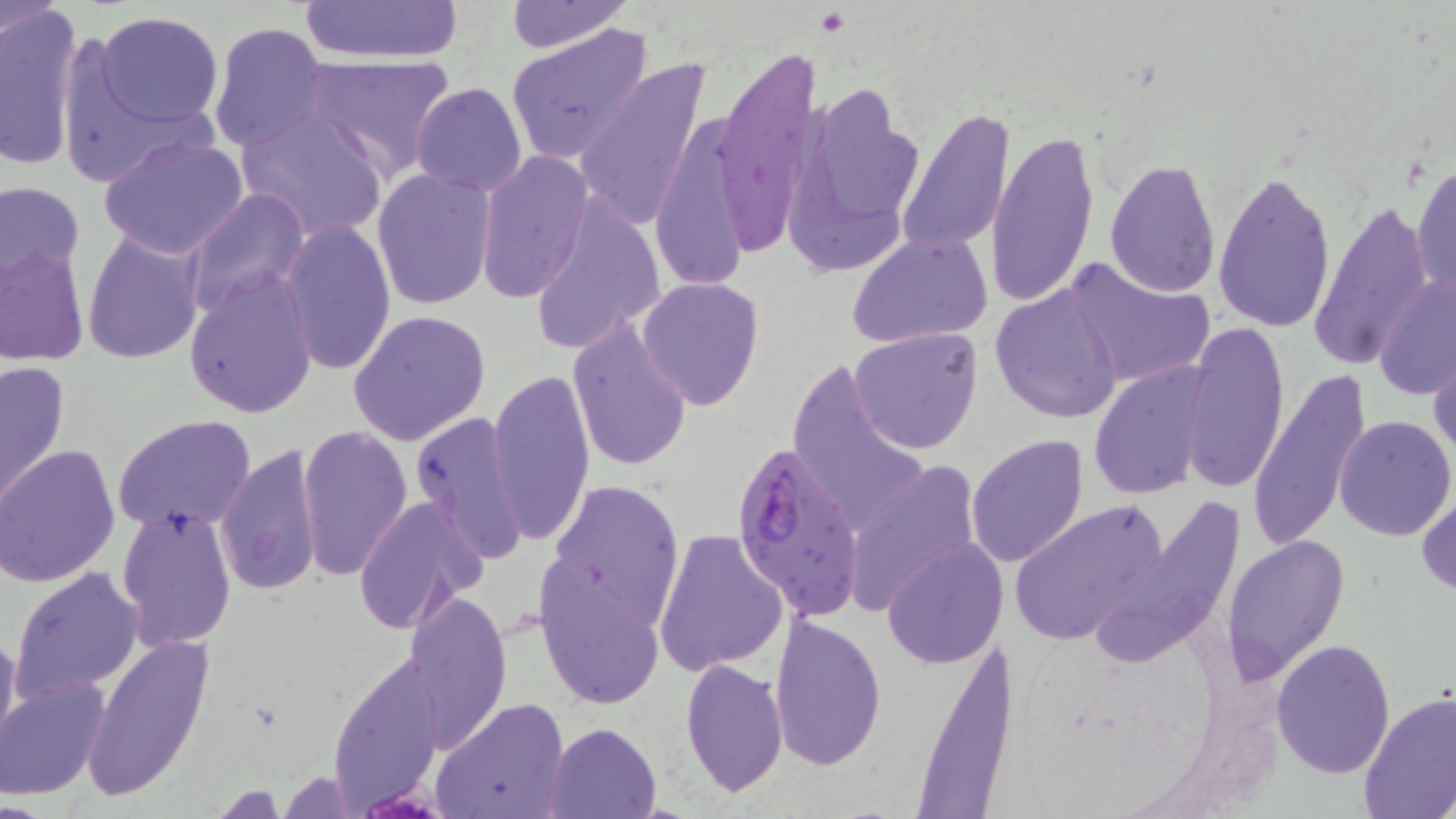

slide-level diagnosis = Plasmodium falciparum
modality = light microscopy
stain = May-Grünwald-Giemsa
magnification = 1000x
platelet locations = approximate bounding boxes as named x1/y1/x2/y2 corners in pixels: (x1=817, y1=8, x2=848, y2=35)
field of view = one of a larger specimen
image size = 1456×819 pixels
uninfected red blood cell locations = approximate bounding boxes as named x1/y1/x2/y2 corners in pixels: (x1=301, y1=0, x2=465, y2=66), (x1=502, y1=1, x2=634, y2=53), (x1=0, y1=2, x2=89, y2=172), (x1=93, y1=11, x2=225, y2=126), (x1=208, y1=21, x2=329, y2=152), (x1=505, y1=23, x2=655, y2=166), (x1=716, y1=48, x2=822, y2=245), (x1=301, y1=52, x2=457, y2=180), (x1=573, y1=58, x2=714, y2=232), (x1=788, y1=80, x2=929, y2=264), (x1=409, y1=83, x2=528, y2=197), (x1=235, y1=108, x2=390, y2=243), (x1=896, y1=108, x2=1018, y2=257), (x1=648, y1=112, x2=771, y2=296), (x1=987, y1=130, x2=1098, y2=308), (x1=98, y1=132, x2=252, y2=260), (x1=476, y1=150, x2=592, y2=303), (x1=1105, y1=158, x2=1221, y2=296), (x1=1412, y1=159, x2=1455, y2=305), (x1=370, y1=166, x2=496, y2=310), (x1=1212, y1=168, x2=1338, y2=333), (x1=0, y1=179, x2=86, y2=295), (x1=182, y1=188, x2=310, y2=319), (x1=523, y1=194, x2=669, y2=356), (x1=1310, y1=202, x2=1433, y2=372), (x1=280, y1=218, x2=395, y2=377), (x1=81, y1=227, x2=204, y2=364), (x1=846, y1=231, x2=993, y2=349), (x1=0, y1=242, x2=89, y2=367), (x1=1061, y1=258, x2=1213, y2=388), (x1=1375, y1=265, x2=1454, y2=406), (x1=183, y1=270, x2=318, y2=420), (x1=637, y1=275, x2=765, y2=409), (x1=990, y1=284, x2=1126, y2=424), (x1=347, y1=309, x2=491, y2=447), (x1=567, y1=317, x2=693, y2=474), (x1=1179, y1=321, x2=1291, y2=493), (x1=850, y1=326, x2=983, y2=454), (x1=1431, y1=342, x2=1456, y2=471), (x1=1, y1=359, x2=71, y2=508), (x1=788, y1=359, x2=929, y2=534), (x1=1088, y1=362, x2=1214, y2=499), (x1=486, y1=364, x2=595, y2=549), (x1=1248, y1=367, x2=1372, y2=548), (x1=407, y1=409, x2=527, y2=561), (x1=112, y1=414, x2=259, y2=535), (x1=1334, y1=414, x2=1454, y2=540), (x1=297, y1=425, x2=413, y2=580), (x1=966, y1=434, x2=1091, y2=568), (x1=216, y1=441, x2=324, y2=596), (x1=0, y1=444, x2=120, y2=587), (x1=839, y1=461, x2=983, y2=616), (x1=546, y1=479, x2=685, y2=628), (x1=1417, y1=490, x2=1456, y2=596), (x1=1093, y1=493, x2=1247, y2=671), (x1=353, y1=496, x2=488, y2=632), (x1=1008, y1=499, x2=1170, y2=645), (x1=116, y1=506, x2=237, y2=651), (x1=653, y1=528, x2=789, y2=676), (x1=1222, y1=531, x2=1349, y2=686), (x1=882, y1=536, x2=1005, y2=668), (x1=534, y1=560, x2=666, y2=710), (x1=10, y1=566, x2=145, y2=702), (x1=402, y1=589, x2=514, y2=752), (x1=767, y1=613, x2=887, y2=771), (x1=0, y1=618, x2=19, y2=755), (x1=79, y1=632, x2=218, y2=801), (x1=1272, y1=638, x2=1396, y2=777), (x1=328, y1=649, x2=447, y2=806), (x1=680, y1=658, x2=789, y2=798), (x1=2, y1=675, x2=109, y2=800), (x1=1357, y1=690, x2=1456, y2=818), (x1=431, y1=697, x2=571, y2=819), (x1=547, y1=721, x2=661, y2=818), (x1=276, y1=771, x2=358, y2=815)
preparation = thin blood smear
Plasmodium falciparum-infected red blood cell locations = approximate bounding boxes as named x1/y1/x2/y2 corners in pixels: (x1=729, y1=437, x2=867, y2=620)